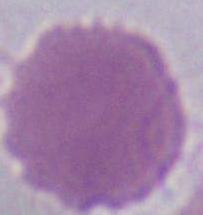
Summary:
  - Identification: red blood cell
  - Magnification: 1000x
  - Modality: photomicrograph